State the blood parasite species.
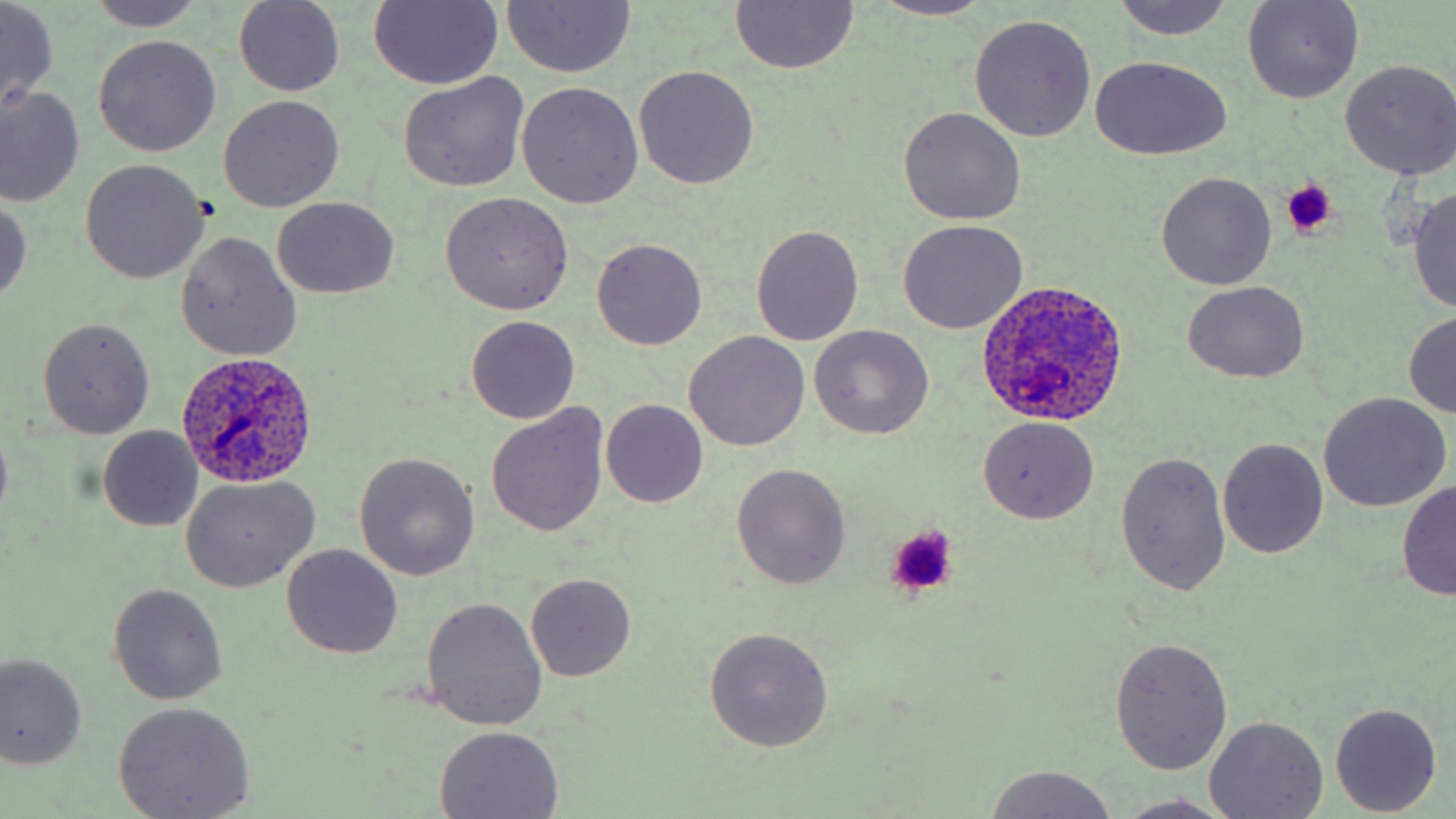
Plasmodium ovale.

Summary:
  - Coordinate format: approximate bounding boxes as (x1,y1)-(x2,y2) corner pairs in pixels
  - Plasmodium ovale-infected red blood cell locations: (975,280)-(1130,429), (179,352)-(319,489)
  - Uninfected red blood cell locations: (88,0)-(206,32), (365,0)-(504,87), (872,0)-(996,20), (0,1)-(59,113), (234,1)-(345,96), (1111,1)-(1233,42), (1242,1)-(1364,105), (502,2)-(635,76), (730,2)-(859,74), (969,14)-(1096,142), (93,35)-(220,155), (1091,55)-(1233,161), (1340,59)-(1456,180), (634,65)-(759,189), (399,73)-(528,191), (517,81)-(642,209), (0,87)-(85,208), (218,96)-(343,211), (899,107)-(1025,225), (80,160)-(209,284), (1156,172)-(1277,290), (1407,186)-(1456,313), (439,192)-(573,314), (0,196)-(31,307), (272,198)-(399,299), (898,219)-(1029,334), (751,225)-(863,345), (175,232)-(301,361), (591,238)-(707,350), (1183,282)-(1311,380), (1404,312)-(1456,417), (466,316)-(580,423), (39,318)-(154,438), (810,325)-(933,440), (684,330)-(809,452), (1319,393)-(1451,510), (601,400)-(707,508), (488,405)-(608,535), (978,415)-(1098,523), (0,421)-(13,525), (97,426)-(205,531), (1218,437)-(1329,559), (1115,451)-(1231,595), (354,453)-(479,580), (731,463)-(852,590), (180,475)-(319,592), (1396,481)-(1456,600), (282,544)-(402,659), (526,573)-(637,682), (108,584)-(227,705), (420,596)-(549,731), (704,627)-(834,752), (1110,636)-(1233,775), (0,653)-(86,769), (113,702)-(256,817), (1329,702)-(1441,816), (1205,716)-(1329,818), (434,724)-(564,818), (982,765)-(1118,818), (1110,792)-(1238,819)
  - Platelet locations: (1278,182)-(1336,237), (882,524)-(960,599)
  - Modality: optical microscopy
  - Magnification: 1000x
  - Stain: May-Grünwald-Giemsa
  - Field of view: one of a larger specimen
  - Preparation: thin blood smear
  - Image size: 1456×819 pixels